Comment on the morphology of the red blood cells.
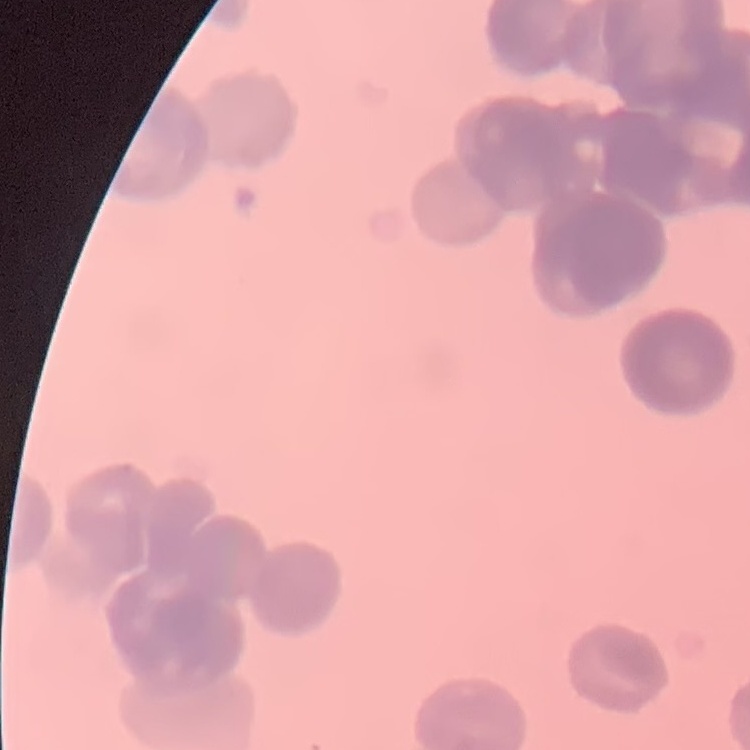
They show rouleaux formation.

Summary:
  - Image type: one tile cut from a larger photomicrograph
  - Stain: Field's or Giemsa
  - Preparation: thin blood film